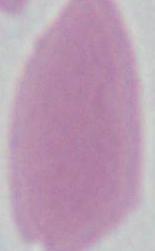

Photomicrograph. A red blood cell is seen. 1000x magnification.